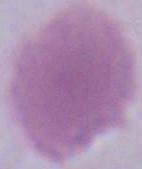

Micrograph. 1000x magnification. A red blood cell is seen.